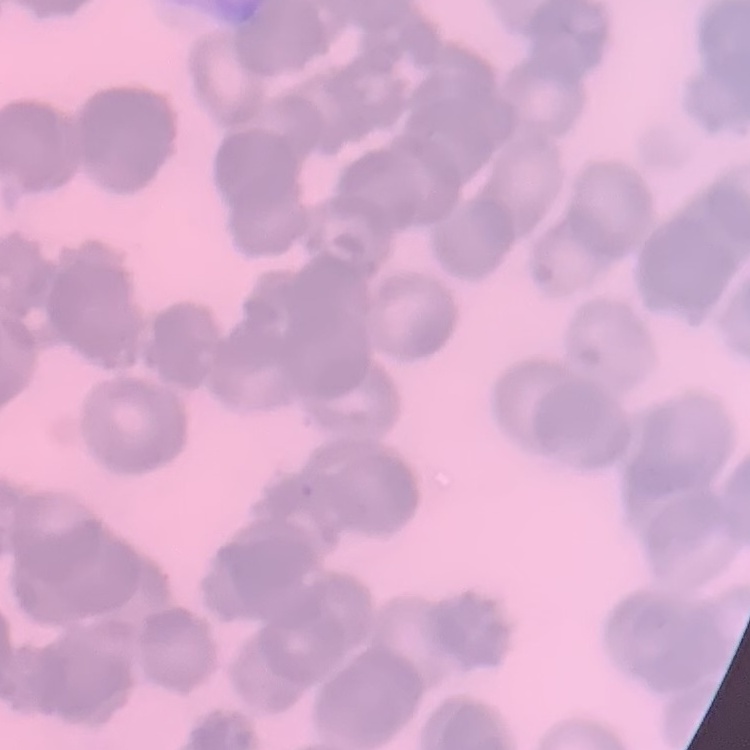
erythrocyte morphology = rouleaux formation
stain = Field's or Giemsa
image type = square crop of a larger photomicrograph
preparation = thin peripheral smear